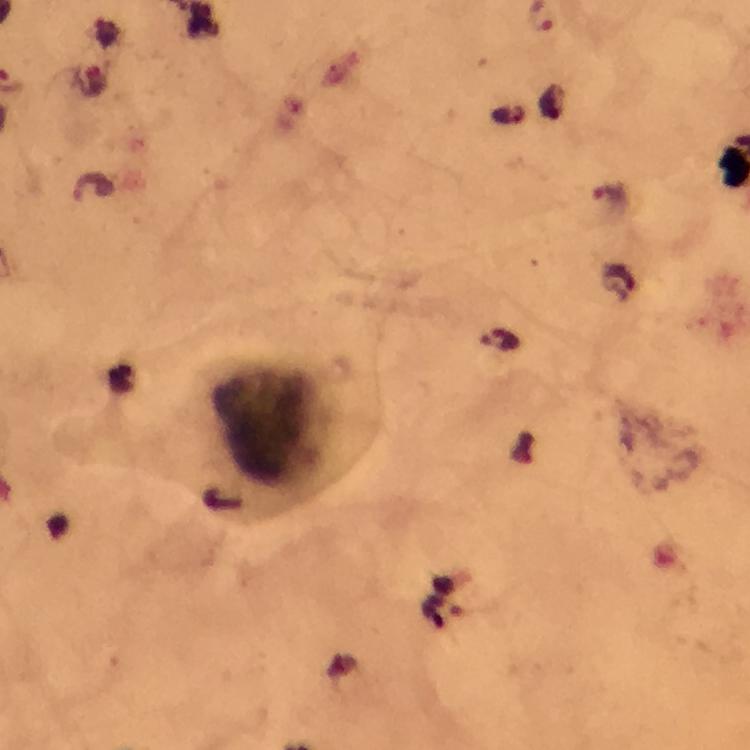

magnification = 100x
cropped from = a single field of view
immersion oil = applied
image size = 750×750 pixels
context = from a malaria diagnostic workup
malaria parasite locations = approximate object centers, in pixels from the top-left corner: (x=93, y=184), (x=609, y=196), (x=499, y=340)
preparation = thick blood film
capture = smartphone camera through the microscope
stain = Giemsa
leukocyte locations = approximate object centers, in pixels from the top-left corner: (x=271, y=424)